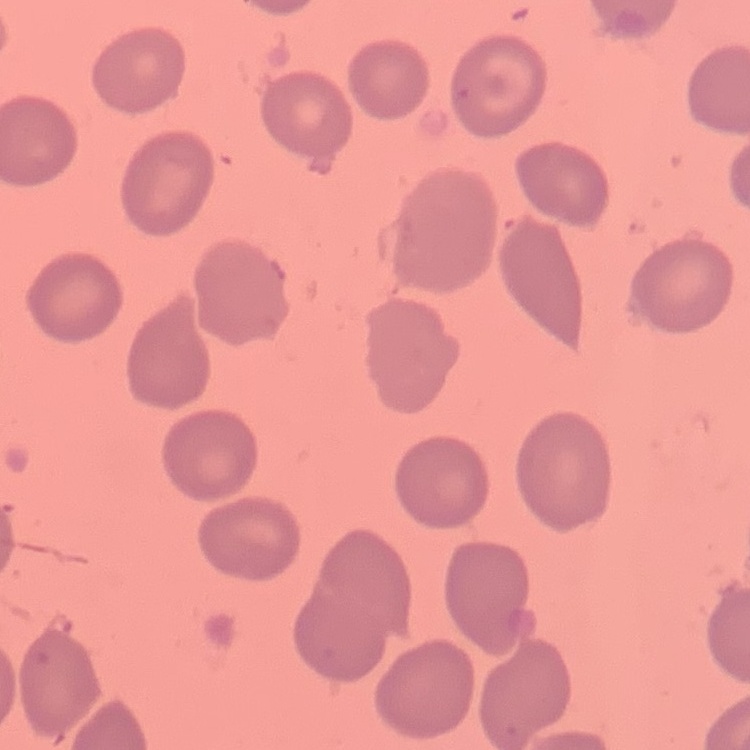

Summary:
  - Red blood cell morphology: no rouleaux formation
  - Preparation: thin peripheral smear
  - Image type: one tile cut from a larger photomicrograph
  - Stain: Field's or Giemsa